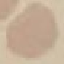
Result: negative for malaria parasites. Thin smear of blood. Acquired by smartphone through the microscope eyepiece. Giemsa-stained preparation. Automatically extracted cell patch, resized to 64 × 64 pixels.